Classify this cell by malaria status.
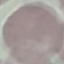
Uninfected.

Acquired by smartphone through the microscope eyepiece. Cell patch, automatically extracted from a larger field of view and resized to 64 × 64 pixels. Thin smear of blood. Giemsa stain.